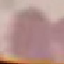 Malaria status: uninfected. Giemsa-stained preparation. Automatically extracted cell patch, resized to 64 × 64 pixels. Photographed with a smartphone camera at the microscope eyepiece. Thin blood film.